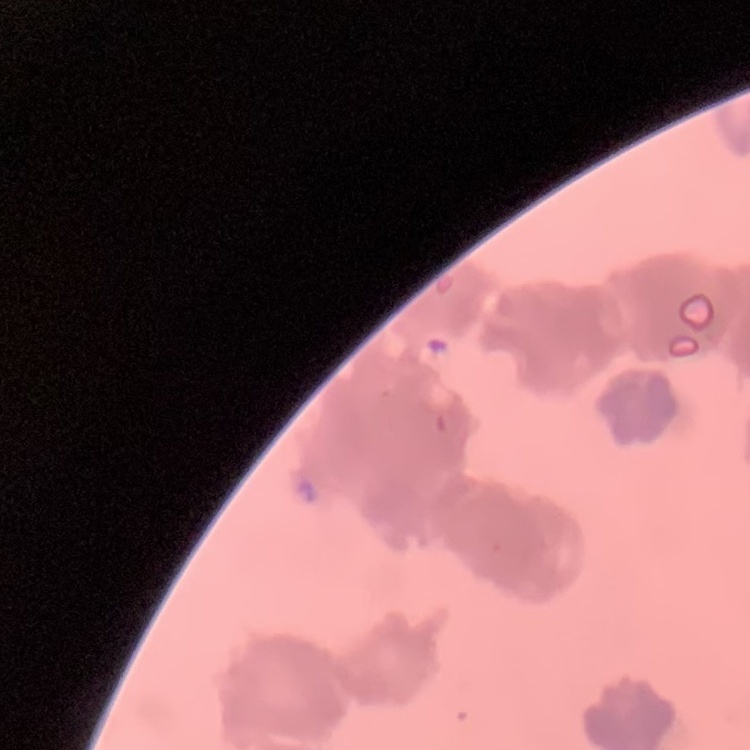

erythrocyte morphology = rouleaux formation
image type = one tile cut from a larger photomicrograph
preparation = thin blood smear
stain = Field's or Giemsa